Evaluate for Plasmodium parasites.
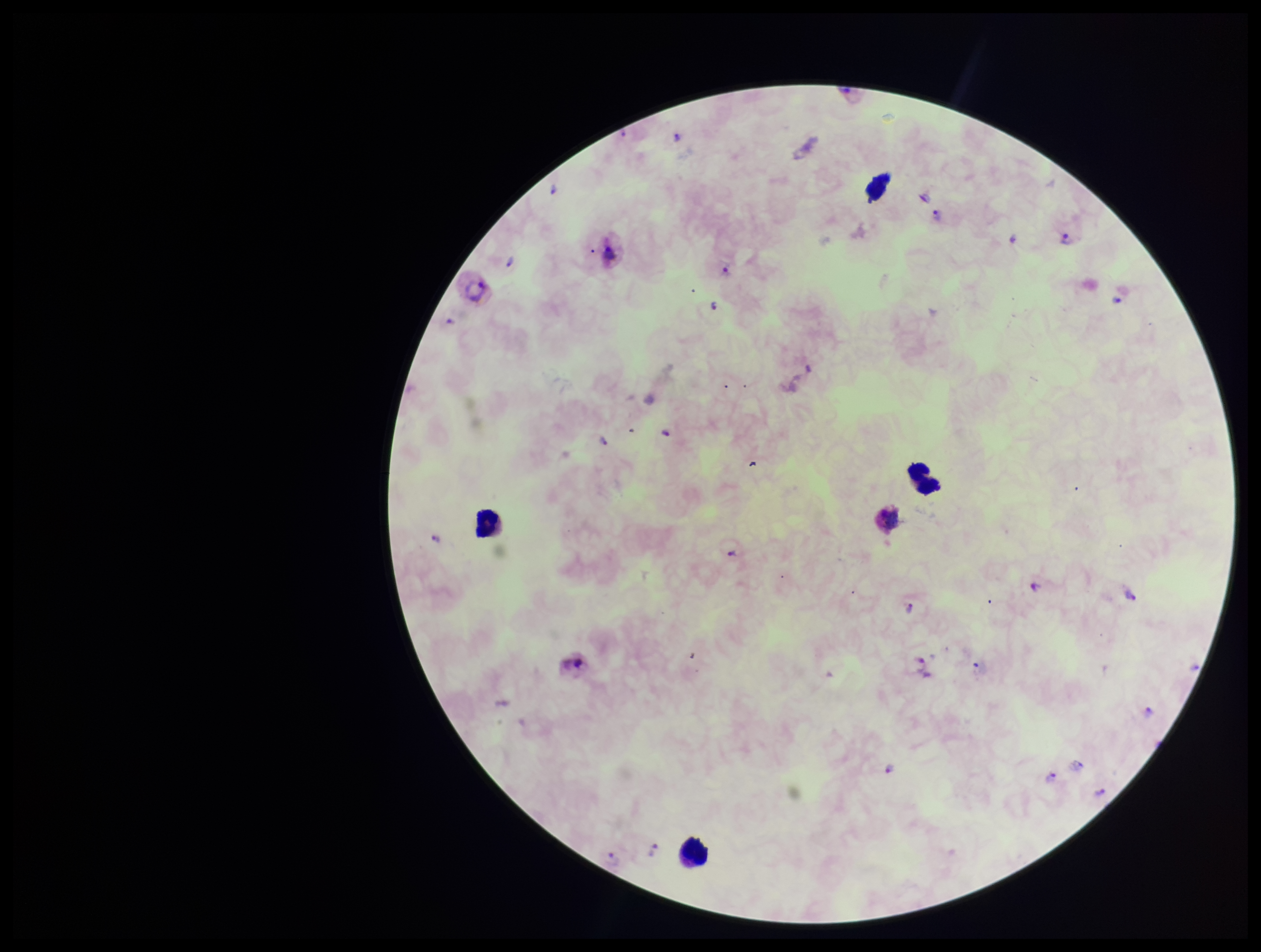
Detected.

Parasite count: 20. Giemsa stain. Preparation: thick smear. Photographed through the microscope eyepiece with a smartphone camera. Single field of view. Image is 1261×952 pixels. Patient malaria status: positive. Leukocyte count: 5. Species reported for this patient: Plasmodium vivax.